Locate every malaria parasite and every leukocyte.
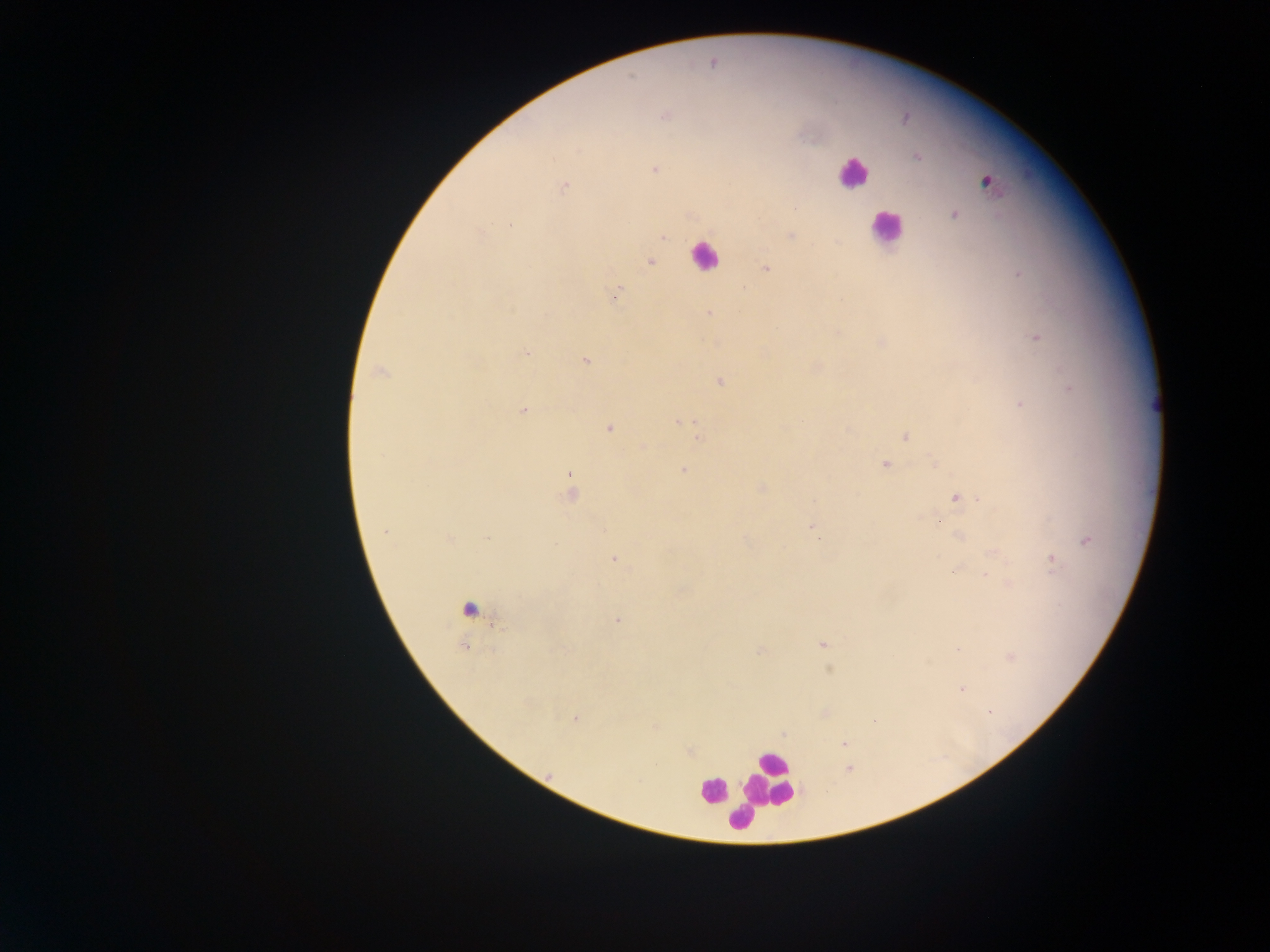

Approximate centers as {x, y} in pixels.
Malaria parasites: {712, 63}, {665, 115}, {918, 157}, {654, 169}, {564, 186}, {954, 214}, {510, 224}, {480, 233}, {790, 236}, {662, 238}, {650, 263}, {765, 270}, {1019, 274}, {618, 289}, {709, 313}, {1036, 338}, {526, 352}, {585, 360}, {380, 372}, {720, 381}, {1069, 388}, {1020, 404}, {523, 410}, {681, 421}, {802, 421}, {608, 429}, {905, 436}, {698, 437}, {935, 463}, {885, 464}, {684, 469}, {570, 474}, {761, 488}, {571, 494}, {957, 498}, {813, 527}, {384, 532}, {959, 536}, {487, 538}, {448, 539}, {1087, 541}, {614, 559}, {1052, 563}, {953, 572}, {985, 574}, {617, 620}, {822, 645}, {958, 649}, {760, 651}, {1011, 657}, {962, 689}, {990, 713}, {575, 719}, {874, 720}, {843, 744}, {848, 769}.
Leukocytes: {852, 174}, {988, 182}, {886, 227}, {703, 255}, {466, 609}, {770, 779}, {711, 790}, {739, 817}.

Image is 1270×952 pixels. Collected in Ghana. Mobile-phone photograph taken through the microscope. One field of view. Thick blood film.